Classify this cell by malaria status.
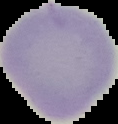

Uninfected.

Summary:
  - Image size: 118×124 pixels
  - Preparation: thin blood film
  - Image type: cell region segmented out of the field of view; surrounding area masked to black